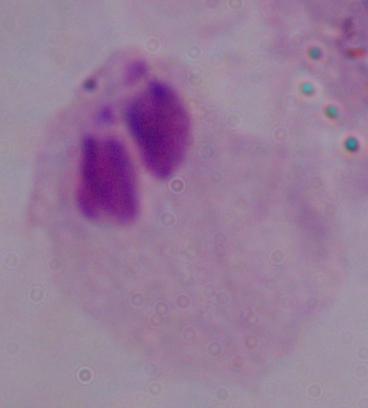

magnification = 1000x
modality = micrograph
identification = trichomonad